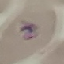

result = malaria parasites detected
image type = cell patch, automatically extracted from a larger field of view and resized to 64 × 64 pixels
preparation = thin blood film
capture = smartphone through the microscope eyepiece
stain = Giemsa